Classify this cell by malaria status.
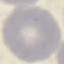

Uninfected.

Cell patch, automatically extracted from a larger field of view and resized to 64 × 64 pixels. Thin blood film. Photographed with a smartphone camera at the microscope eyepiece. Giemsa-stained preparation.